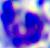

{
  "magnification": "400x",
  "identification": "leukocyte",
  "modality": "photomicrograph"
}